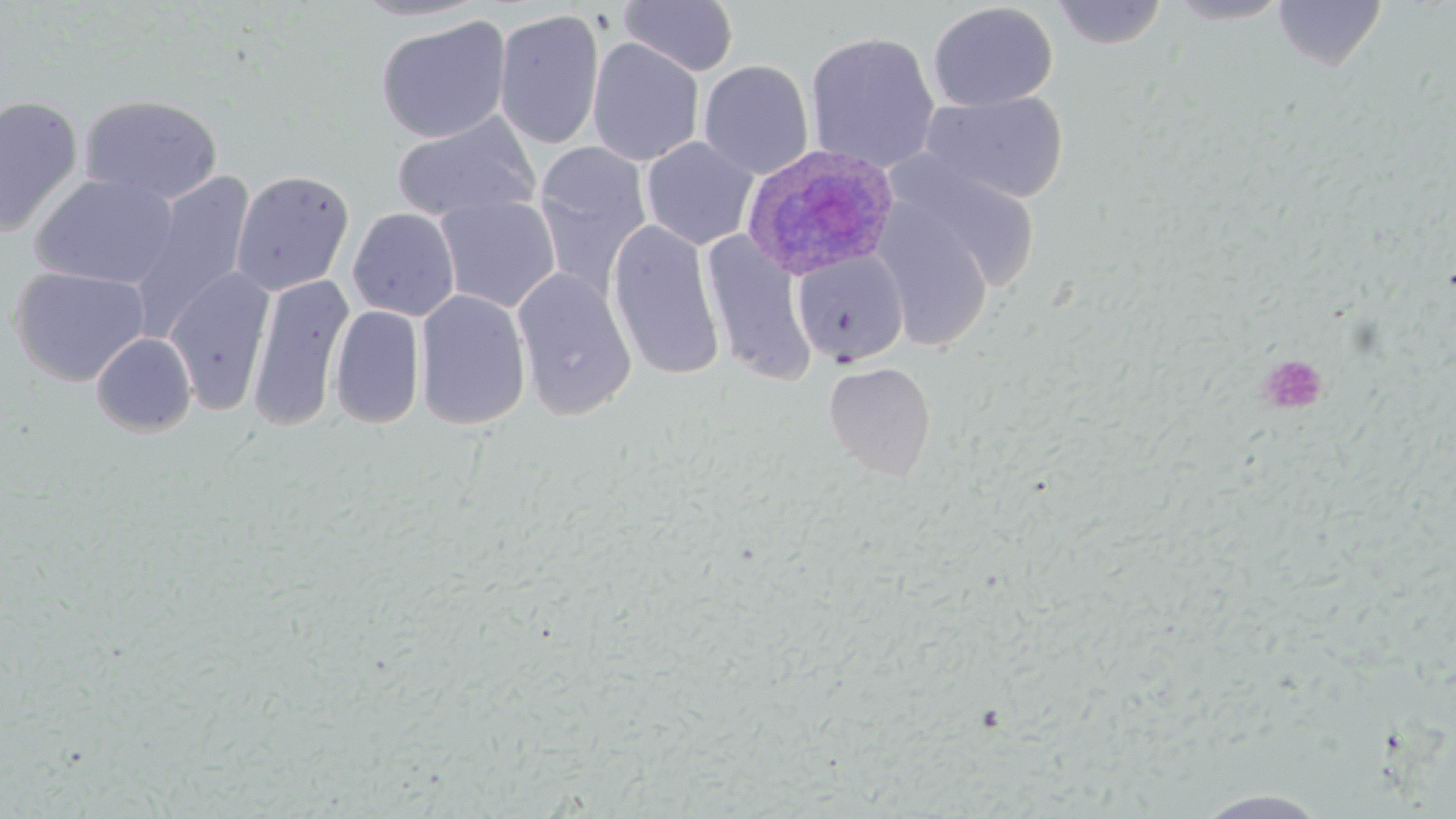
Summary:
  - Coordinate format: approximate bounding boxes as (x1,y1)-(x2,y2) corner pairs in pixels
  - Uninfected red blood cell locations: (351,0)-(491,23), (1050,0)-(1168,49), (1165,0)-(1291,25), (619,1)-(739,77), (1272,1)-(1387,71), (927,2)-(1058,111), (493,8)-(605,150), (376,15)-(511,143), (804,31)-(941,173), (587,37)-(704,166), (698,59)-(814,179), (918,91)-(1069,205), (78,93)-(223,205), (0,94)-(83,238), (392,112)-(541,223), (640,136)-(758,250), (532,141)-(653,297), (889,157)-(1043,296), (231,169)-(354,296), (31,172)-(179,289), (129,172)-(255,341), (435,195)-(561,314), (875,204)-(994,352), (348,207)-(460,321), (606,220)-(725,382), (700,232)-(816,384), (792,250)-(909,366), (9,265)-(151,387), (165,266)-(275,416), (511,267)-(637,421), (247,273)-(354,431), (414,289)-(531,430), (329,304)-(426,429), (91,331)-(197,437), (824,361)-(936,480), (1190,788)-(1334,818)
  - Plasmodium ovale-infected red blood cell locations: (739,143)-(900,282)
  - Platelet locations: (1256,353)-(1329,415)
  - Slide-level diagnosis: Plasmodium ovale
  - Stain: May-Grünwald-Giemsa
  - Preparation: thin blood smear
  - Magnification: 1000x
  - Image size: 1456×819 pixels
  - Field of view: single
  - Modality: light microscopy